Assess this cell for malaria.
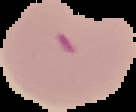

It is parasitized.

Summary:
  - Preparation: thin blood smear
  - Image size: 136×112 pixels
  - Image type: cell region segmented out of the field of view; surrounding area masked to black